Identify the blood parasite species.
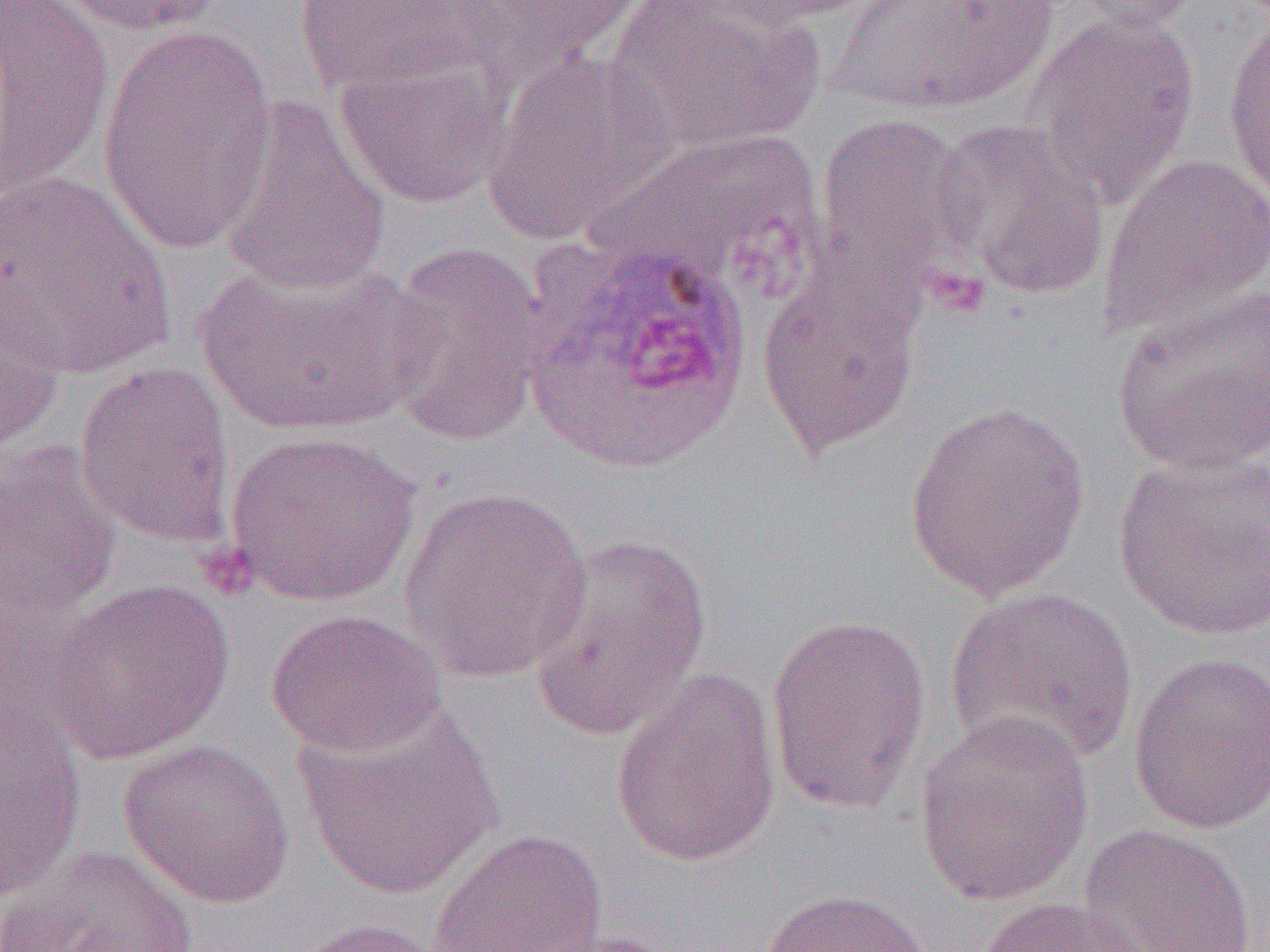
Plasmodium ovale.

Approximate bounding boxes as (x1,y1)-(x2,y2) corner pairs in pixels. Uninfected red blood cell locations: (0,0)-(115,200), (49,0)-(232,37), (604,0)-(823,153), (697,0)-(885,29), (832,0)-(1057,117), (1067,0)-(1208,34), (294,1)-(487,95), (436,1)-(647,81), (1026,12)-(1200,208), (1222,13)-(1270,212), (96,27)-(276,254), (481,48)-(678,247), (334,49)-(511,210), (217,98)-(393,297), (811,113)-(981,298), (932,119)-(1111,300), (592,128)-(822,296), (1098,153)-(1270,337), (0,172)-(176,380), (380,241)-(550,447), (193,259)-(434,439), (755,262)-(924,458), (0,272)-(66,453), (1111,289)-(1270,477), (75,361)-(237,549), (903,401)-(1091,600), (225,430)-(422,607), (0,442)-(120,630), (1113,453)-(1269,641), (398,486)-(594,682), (526,530)-(712,744), (44,577)-(235,766), (944,586)-(1138,770), (265,608)-(445,758), (765,615)-(932,815), (1127,651)-(1270,836), (610,668)-(782,867), (296,701)-(504,900), (0,705)-(87,900), (913,710)-(1096,907), (117,738)-(297,908), (1077,823)-(1257,952), (427,828)-(608,952), (1,845)-(199,952), (758,888)-(933,952), (975,896)-(1150,952), (284,917)-(449,952). Platelet locations: (926,267)-(991,319), (196,541)-(260,600). Plasmodium ovale-infected red blood cell locations: (522,233)-(755,475). Optical microscopy. Thin blood smear. Captured at 1000x magnification. Image is 1270×952 pixels. One field of a larger specimen.